Locate every blood parasite and identify its species.
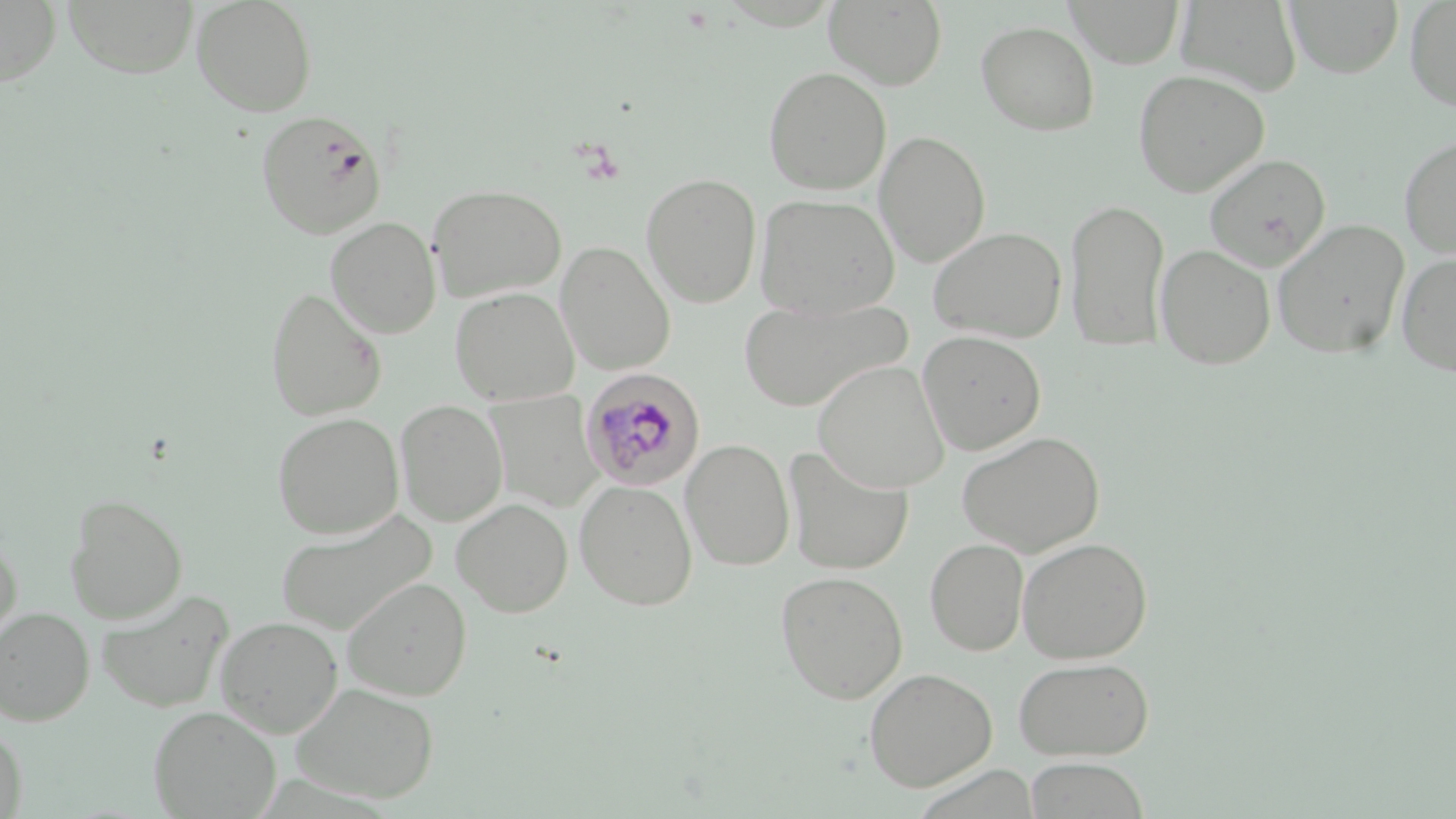
Approximate bounding boxes as (x1, y1, x2, y2) in pixels.
Plasmodium malariae-infected red blood cells: (579, 368, 705, 489).
No Plasmodium falciparum, Plasmodium ovale, Plasmodium vivax, Babesia divergens, or Trypanosoma brucei observed.

slide-level diagnosis = Plasmodium malariae
preparation = thin blood film
modality = light microscopy
field of view = one of a larger specimen
magnification = 1000x
uninfected red blood cell locations = approximate bounding boxes as (x1, y1, x2, y2) in pixels: (0, 0, 61, 87), (63, 0, 198, 78), (192, 0, 318, 117), (1065, 0, 1184, 68), (1286, 0, 1403, 78), (1404, 0, 1456, 112), (824, 1, 947, 90), (1176, 1, 1302, 97), (975, 20, 1100, 136), (763, 66, 891, 196), (1133, 70, 1269, 197), (256, 109, 387, 239), (874, 130, 991, 268), (1399, 134, 1456, 260), (1204, 154, 1330, 270), (641, 173, 762, 307), (427, 184, 567, 303), (754, 193, 898, 321), (1064, 198, 1170, 351), (325, 217, 441, 339), (1272, 219, 1410, 359), (928, 226, 1067, 344), (556, 241, 674, 375), (1155, 244, 1276, 369), (1396, 252, 1456, 378), (265, 287, 386, 422), (450, 287, 579, 406), (737, 296, 909, 412), (917, 331, 1046, 455), (812, 359, 950, 493), (486, 391, 603, 513), (395, 399, 508, 526), (272, 412, 403, 539), (956, 430, 1105, 557), (681, 439, 795, 571), (783, 447, 912, 576), (574, 480, 697, 610), (64, 493, 187, 623), (452, 498, 573, 617), (274, 508, 437, 637), (0, 531, 23, 651), (1016, 536, 1152, 664), (925, 538, 1029, 656), (775, 570, 908, 704), (342, 577, 472, 701), (96, 589, 235, 714), (0, 608, 94, 725), (215, 616, 343, 737), (1012, 656, 1155, 761), (863, 667, 997, 791), (290, 682, 439, 804), (148, 705, 281, 819), (0, 725, 28, 819), (1023, 757, 1152, 818)
stain = May-Grünwald-Giemsa
image size = 1456×819 pixels